Point out each Plasmodium parasite.
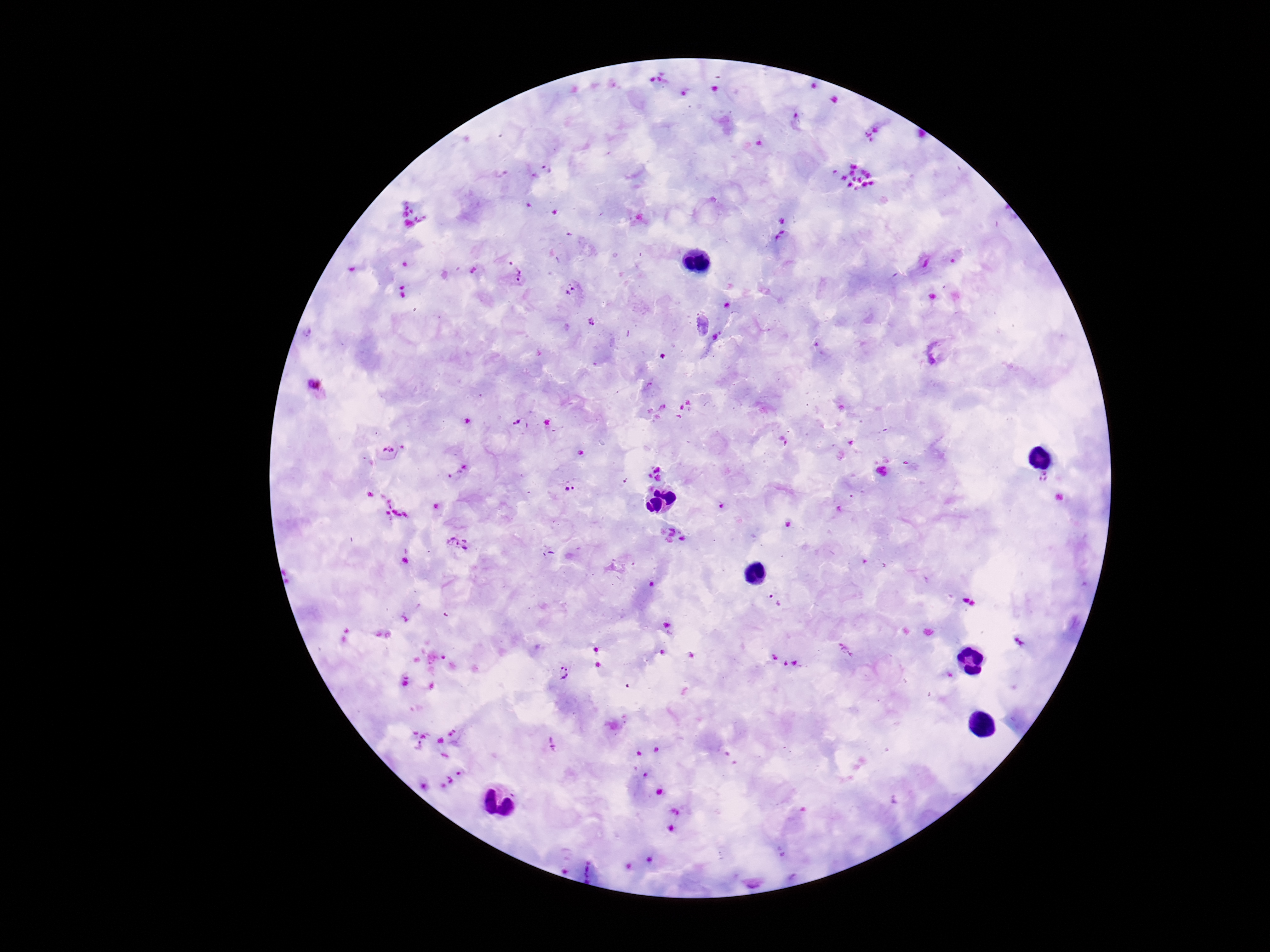
Approximate object centers, in pixels from the top-left corner.
Plasmodium parasites: (x=518, y=277), (x=571, y=291), (x=591, y=321), (x=718, y=337), (x=316, y=386), (x=518, y=422), (x=388, y=450), (x=655, y=474), (x=1044, y=477), (x=569, y=487), (x=722, y=506), (x=788, y=524), (x=682, y=538), (x=456, y=542), (x=775, y=600), (x=563, y=671), (x=552, y=745).

One field from this slide. 100x magnification. Patient malaria status: infected. Image is 1270×952 pixels. Photographed through the microscope eyepiece with a smartphone camera. Giemsa-stained preparation. Thick blood smear.